Assess the morphology of the red blood cells.
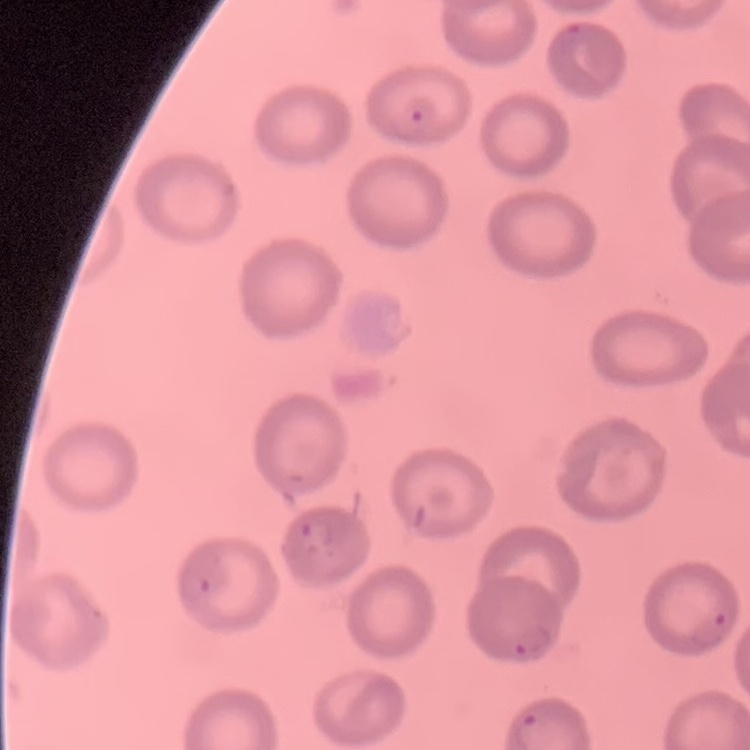

They show no rouleaux formation.

Summary:
  - Preparation: thin peripheral smear
  - Stain: Field's or Giemsa
  - Image type: one tile cut from a larger photomicrograph